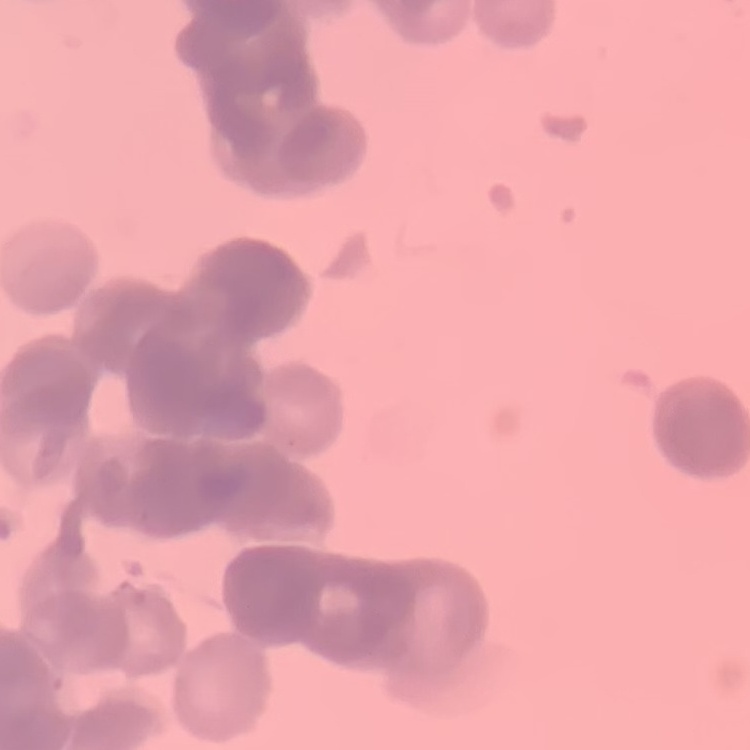

The erythrocytes exhibit rouleaux formation. Field's or Giemsa stain. Thin blood film. One tile cut from a larger photomicrograph.